Describe the morphology of the erythrocytes.
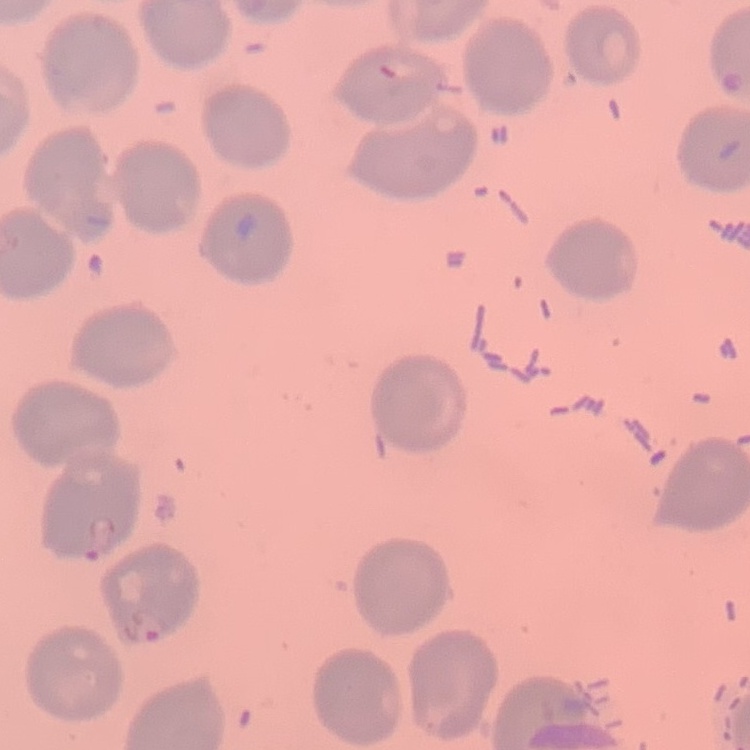

No rouleaux formation.

One tile cut from a larger photomicrograph. Field's or Giemsa stain. Thin peripheral smear.